Classify this cell by malaria status.
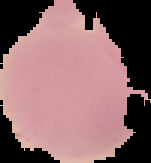
It is uninfected.

Cell region segmented out of the field of view; the surrounding area is masked to black. Image is 151×163 pixels. From a thin blood smear.